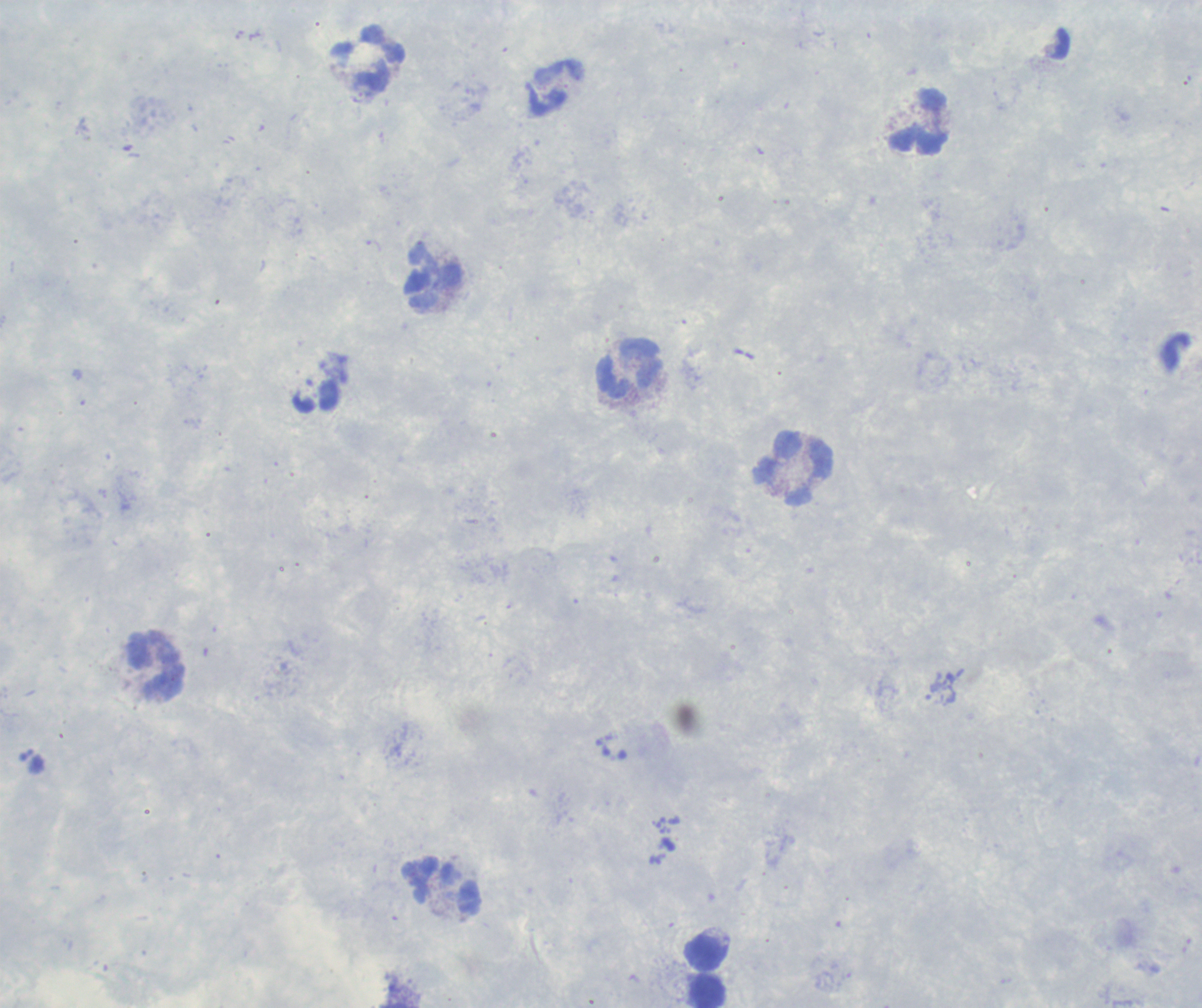

coordinate format = approximate centers as (x, y) in pixels
leukocyte locations = (369, 61), (555, 89), (921, 122), (431, 277), (630, 369), (791, 470), (156, 666), (444, 887), (705, 953), (709, 991)
result = no Plasmodium parasites detected
field of view = single
preparation = thick blood film
coloration quality = good
context = previously used in an actual diagnosis
image size = 1202×1008 pixels
background quality = poor
magnification = 100x
stain = Romanowsky